Identify the preparation type.
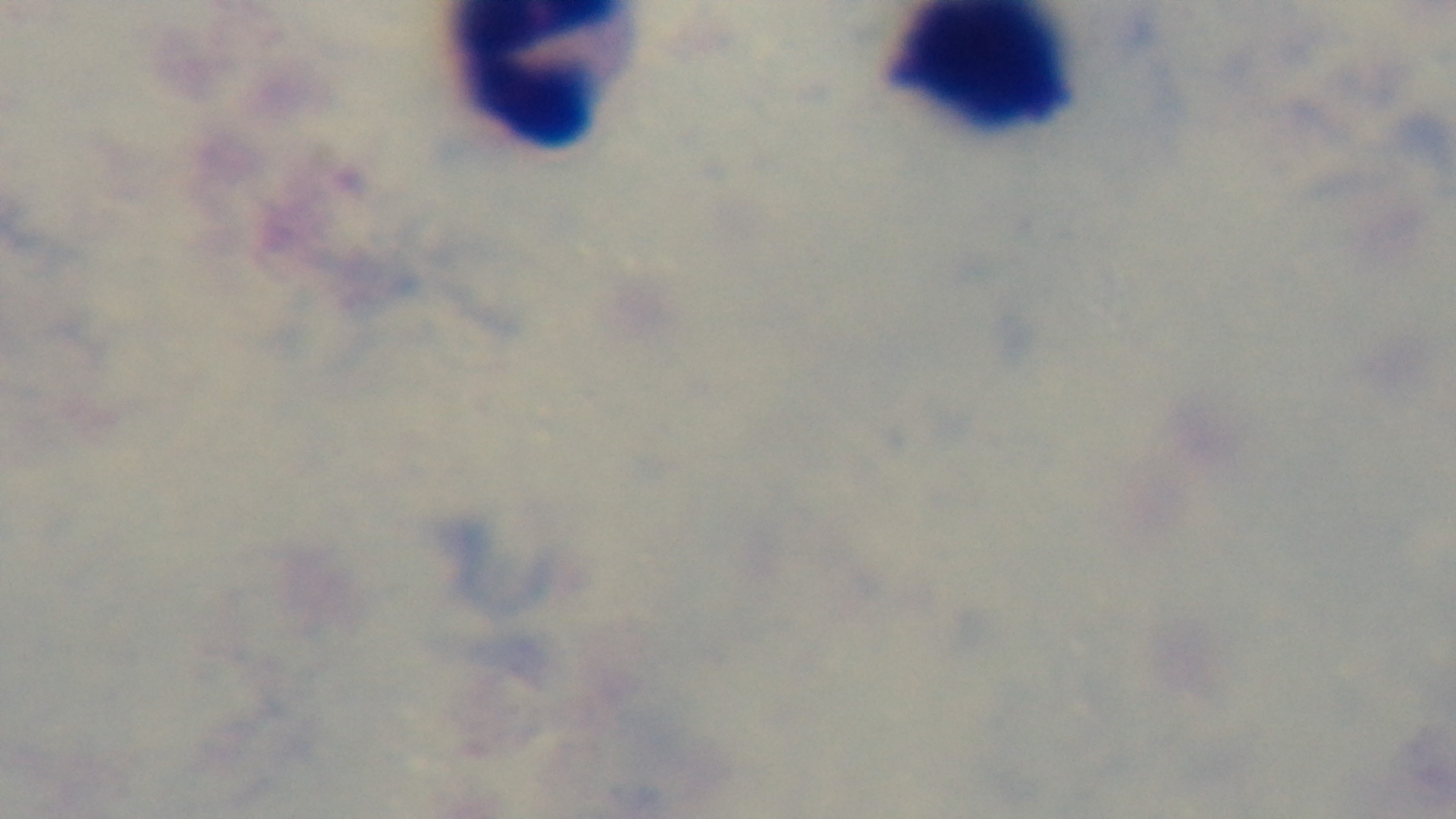
Thick.

malaria_status: negative
capture: mounted 4K digital camera
modality: light microscopy
stain: Giemsa
field_of_view: single
objective: 100x oil immersion